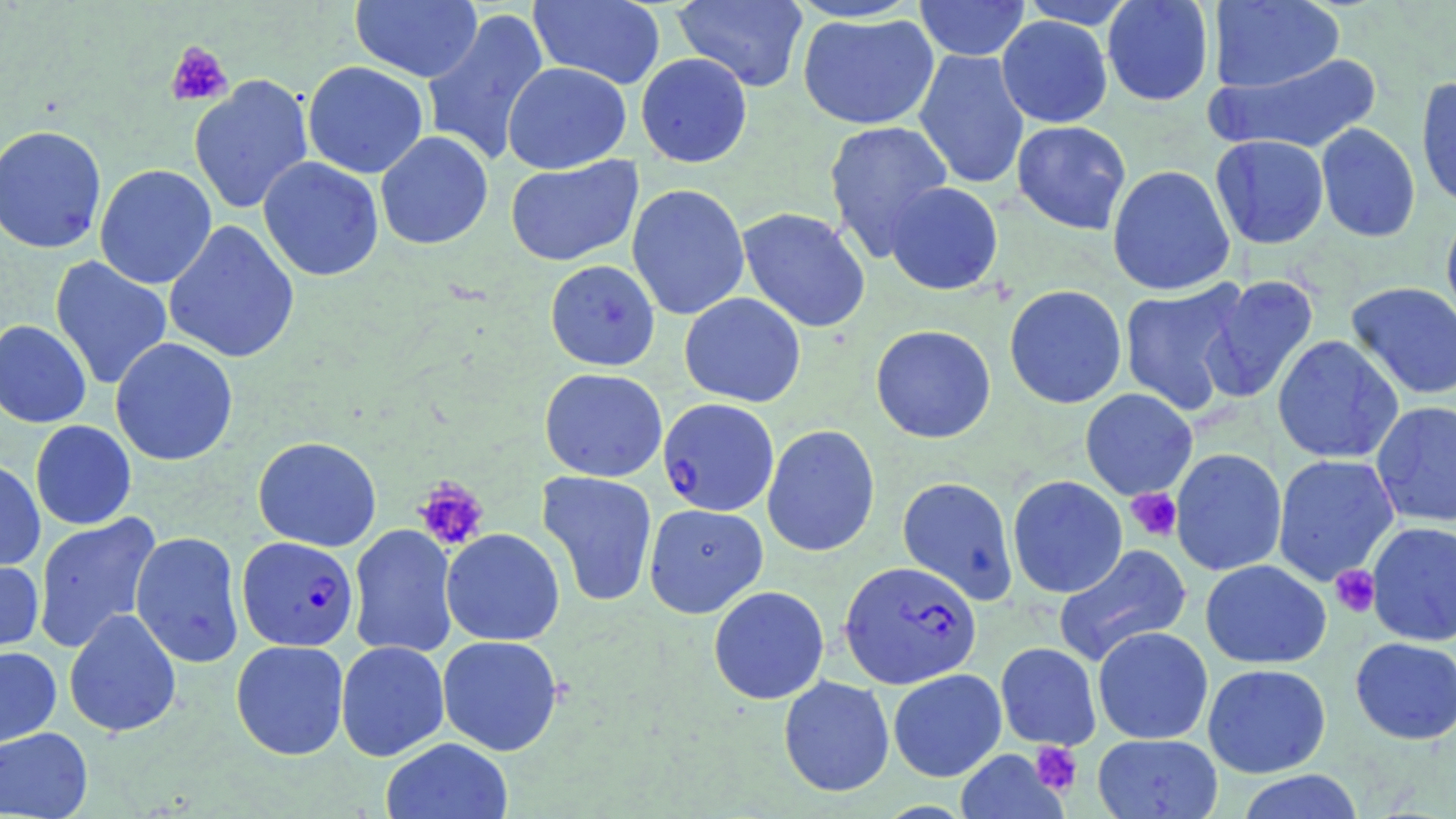
Summary:
  - Coordinate format: approximate bounding boxes as (x1,y1)-(x2,y2) corner pairs in pixels
  - Plasmodium falciparum-infected red blood cell locations: (658,398)-(779,516), (236,536)-(359,651), (840,560)-(981,688)
  - Uninfected red blood cell locations: (350,0)-(483,83), (528,0)-(665,90), (672,0)-(809,92), (1017,0)-(1140,28), (1101,0)-(1215,106), (913,1)-(1031,61), (1207,1)-(1344,94), (421,7)-(550,168), (798,12)-(940,131), (996,15)-(1112,128), (913,49)-(1030,189), (635,52)-(753,168), (1209,52)-(1381,154), (302,61)-(428,178), (502,61)-(632,174), (189,74)-(313,215), (1415,76)-(1456,211), (823,120)-(954,260), (1011,120)-(1131,235), (1316,123)-(1421,242), (0,124)-(107,254), (375,131)-(493,250), (1210,135)-(1330,249), (505,156)-(643,266), (258,157)-(384,281), (94,164)-(217,289), (1108,165)-(1235,295), (884,181)-(1003,295), (626,183)-(750,320), (737,206)-(871,333), (1440,208)-(1456,332), (163,220)-(300,364), (50,256)-(173,391), (544,259)-(661,372), (1201,275)-(1319,404), (1118,280)-(1251,416), (1346,282)-(1456,399), (1004,285)-(1127,409), (679,292)-(806,407), (0,320)-(92,428), (870,324)-(996,443), (1272,335)-(1404,464), (110,337)-(238,466), (540,368)-(667,482), (1080,388)-(1198,500), (1371,401)-(1456,526), (30,420)-(137,529), (762,424)-(880,557), (253,436)-(381,552), (1170,448)-(1287,576), (1272,454)-(1400,586), (0,458)-(46,571), (537,470)-(658,608), (1007,475)-(1128,598), (897,477)-(1018,604), (643,503)-(768,618), (33,511)-(162,653), (1366,521)-(1456,647), (348,523)-(459,659), (441,528)-(565,646), (130,530)-(245,667), (1052,543)-(1193,667), (0,556)-(44,659), (1200,559)-(1332,669), (708,586)-(829,705), (63,608)-(182,738), (1092,626)-(1213,745), (437,635)-(563,756), (1350,637)-(1456,745), (230,640)-(349,760), (335,640)-(450,761), (996,642)-(1101,749), (0,647)-(62,749), (1202,663)-(1331,778), (888,668)-(1007,782), (778,675)-(895,798), (0,726)-(93,818), (1092,733)-(1223,818), (381,737)-(513,819), (955,748)-(1068,819), (1235,770)-(1365,819)
  - Platelet locations: (165,40)-(234,108), (413,477)-(490,552), (1126,488)-(1182,542), (1330,565)-(1380,618), (1029,741)-(1082,796)
  - Slide-level diagnosis: Plasmodium falciparum
  - Image size: 1456×819 pixels
  - Preparation: thin blood film
  - Modality: optical microscopy
  - Field of view: one of a larger specimen
  - Stain: May-Grünwald-Giemsa
  - Magnification: 1000x